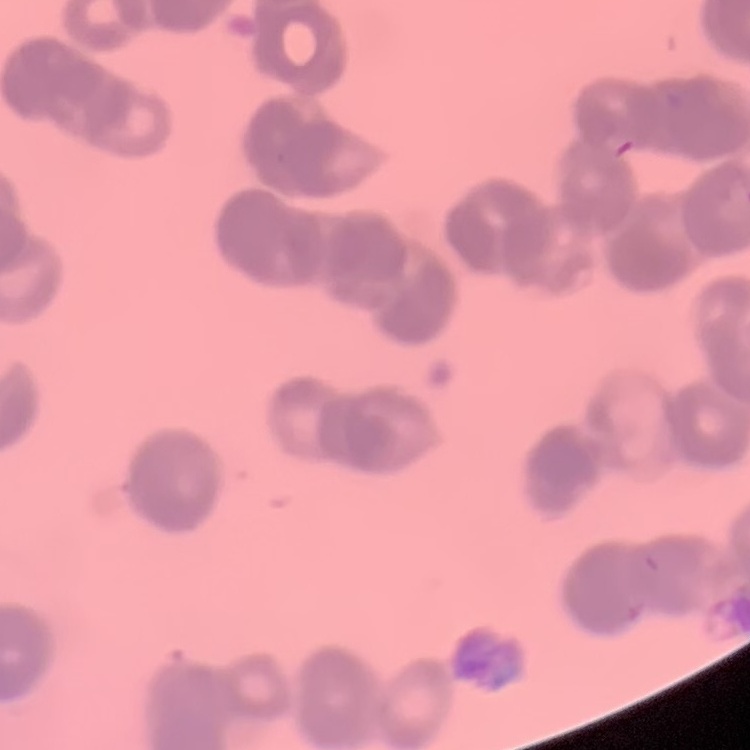
red blood cell morphology = rouleaux formation
image type = square crop of a larger photomicrograph
preparation = thin blood film
stain = Field's or Giemsa